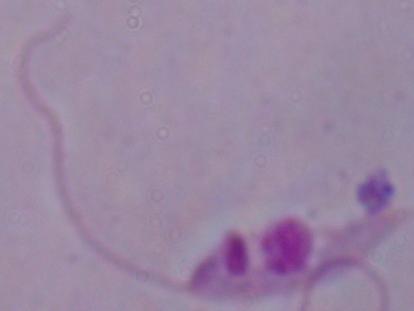 A Leishmania parasite is seen. Photomicrograph. 1000x magnification.